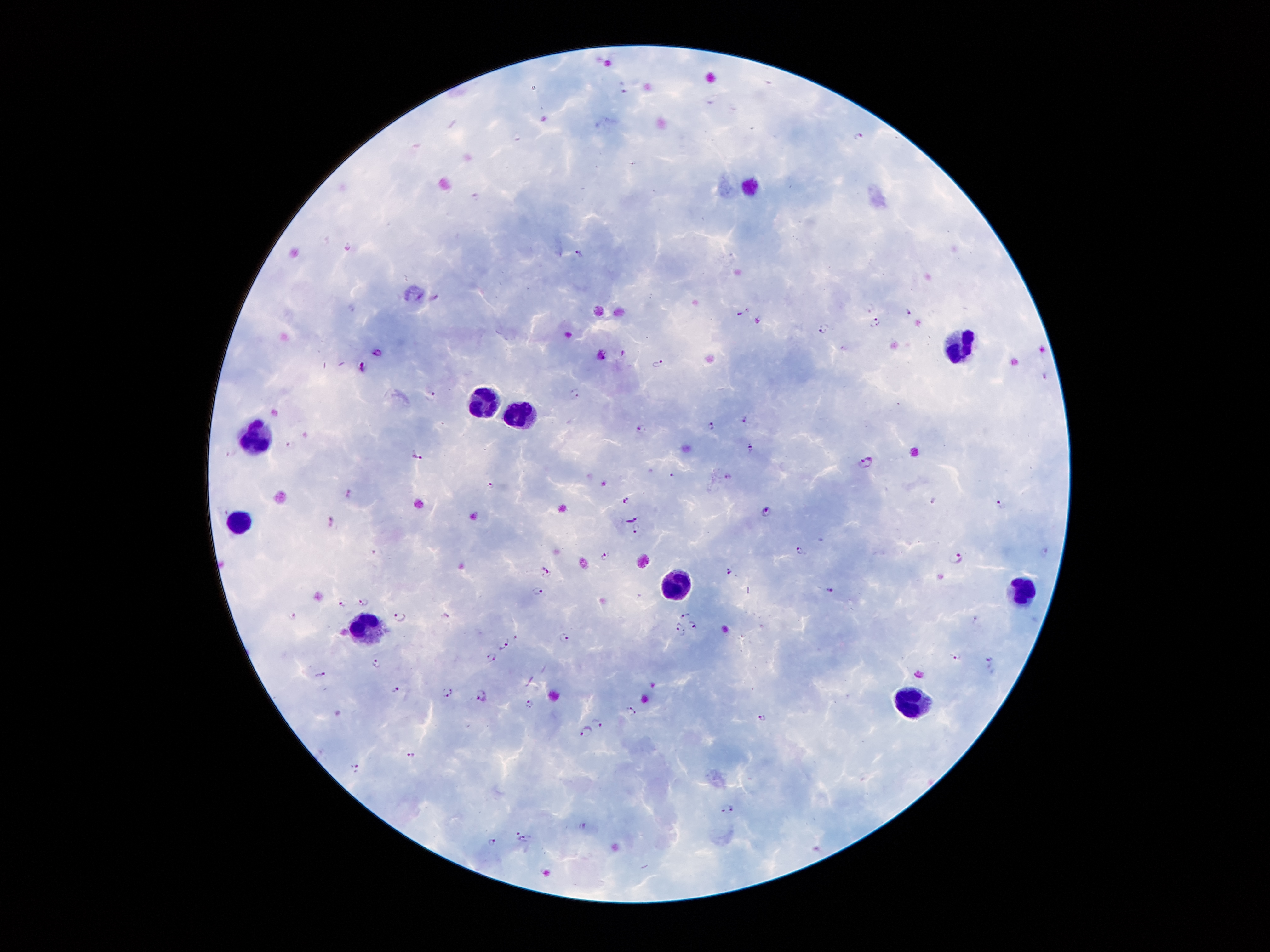
Approximate centers as {x, y} in pixels.
Summary:
  - Leukocyte locations: {960, 344}, {479, 401}, {524, 414}, {260, 433}, {240, 518}, {676, 586}, {1022, 588}, {372, 628}, {914, 702}
  - Plasmodium parasite locations: {623, 88}, {861, 137}, {476, 197}, {347, 244}, {579, 255}, {871, 308}, {745, 311}, {908, 311}, {760, 320}, {877, 322}, {825, 327}, {378, 353}, {658, 361}, {363, 366}, {575, 393}, {430, 397}, {744, 419}, {711, 426}, {643, 429}, {290, 445}, {751, 448}, {418, 455}, {866, 463}, {672, 474}, {729, 476}, {489, 485}, {349, 492}, {626, 501}, {1001, 503}, {767, 511}, {631, 520}, {331, 521}, {637, 526}, {800, 549}, {1045, 553}, {603, 555}, {956, 556}, {547, 573}, {731, 573}, {537, 590}, {831, 592}, {363, 600}, {342, 603}, {291, 616}, {399, 616}, {686, 616}, {978, 620}, {694, 626}, {680, 629}, {564, 637}, {506, 644}, {491, 657}, {955, 657}, {376, 661}, {990, 661}, {321, 674}, {395, 687}, {448, 693}, {480, 695}, {529, 704}, {633, 711}, {764, 718}, {597, 722}, {586, 732}, {413, 756}, {355, 768}, {727, 808}, {583, 826}, {523, 838}, {492, 840}
  - Magnification: 100x
  - Stain: Giemsa
  - Preparation: thick peripheral-blood smear
  - Field of view: single
  - Patient malaria status: positive for Plasmodium falciparum
  - Capture: smartphone camera through the microscope eyepiece
  - Image size: 1270×952 pixels